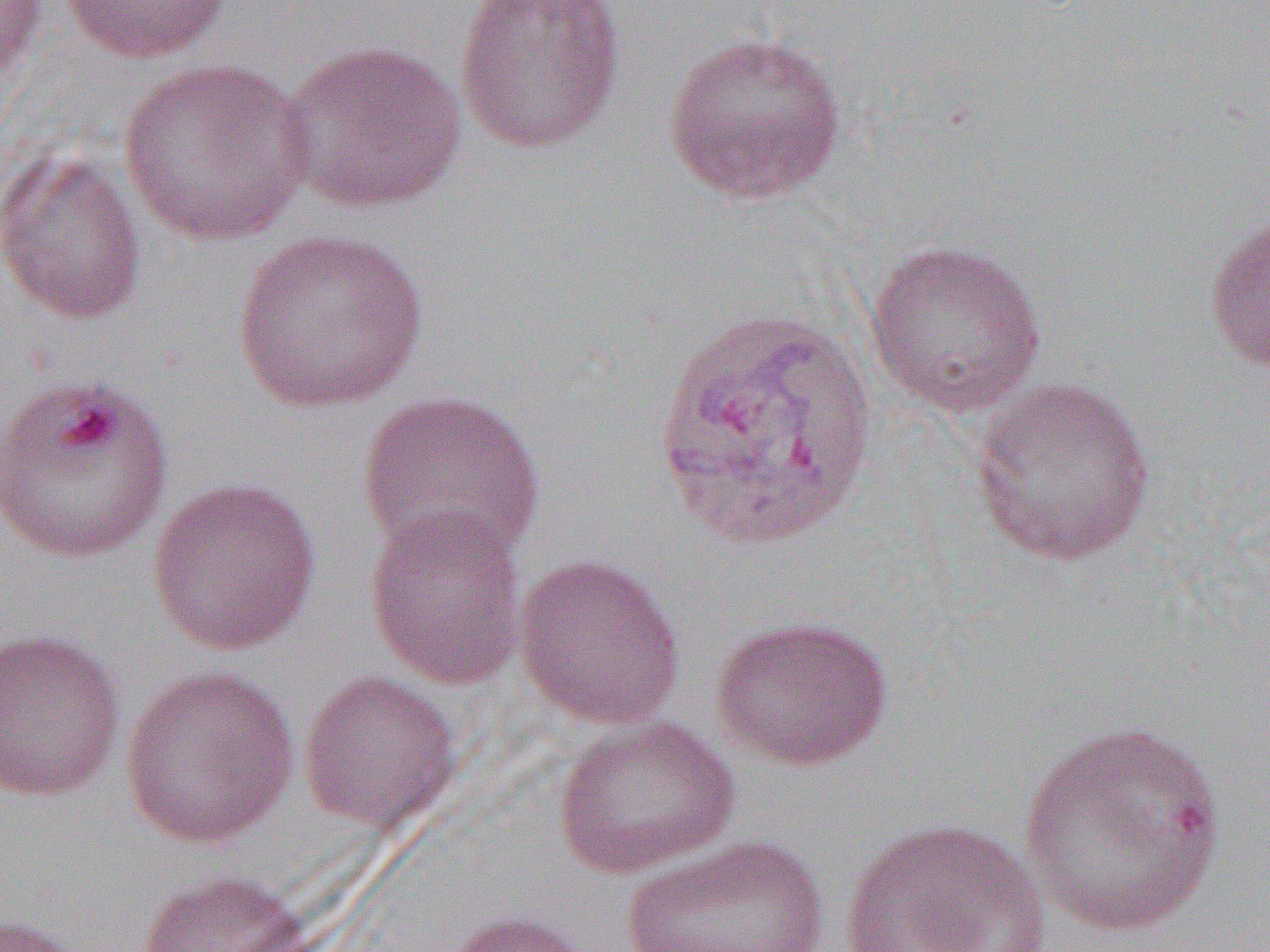

slide-level diagnosis = Plasmodium vivax
image size = 1270×952 pixels
uninfected red blood cell locations = approximate bounding boxes as (x1, y1, x2, y2) in pixels: (0, 0, 49, 93), (58, 0, 235, 64), (453, 0, 626, 155), (661, 30, 847, 205), (277, 39, 468, 214), (116, 58, 316, 248), (1, 145, 148, 326), (1203, 205, 1270, 375), (230, 228, 430, 415), (863, 239, 1047, 418), (0, 371, 176, 563), (967, 375, 1158, 567), (356, 390, 546, 565), (146, 476, 323, 655), (363, 504, 529, 691), (513, 553, 685, 729), (710, 614, 894, 772), (0, 627, 126, 802), (118, 663, 300, 849), (297, 669, 462, 835), (551, 714, 740, 881), (1015, 718, 1230, 939), (839, 816, 1052, 952), (618, 834, 833, 952), (135, 868, 309, 952), (443, 910, 596, 952), (0, 914, 88, 952)
modality = light microscopy
preparation = thin blood smear
magnification = 1000x
field of view = single